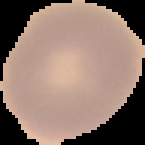

Summary:
  - Image type: segmented cell region with the area outside set to black
  - Image size: 145×145 pixels
  - Preparation: thin blood smear
  - Malaria status: uninfected